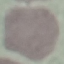
Malaria status: uninfected. Cell patch, automatically extracted from a larger field of view and resized to 64 × 64 pixels. Thin blood film. Giemsa stain. Acquired by smartphone through the microscope eyepiece.